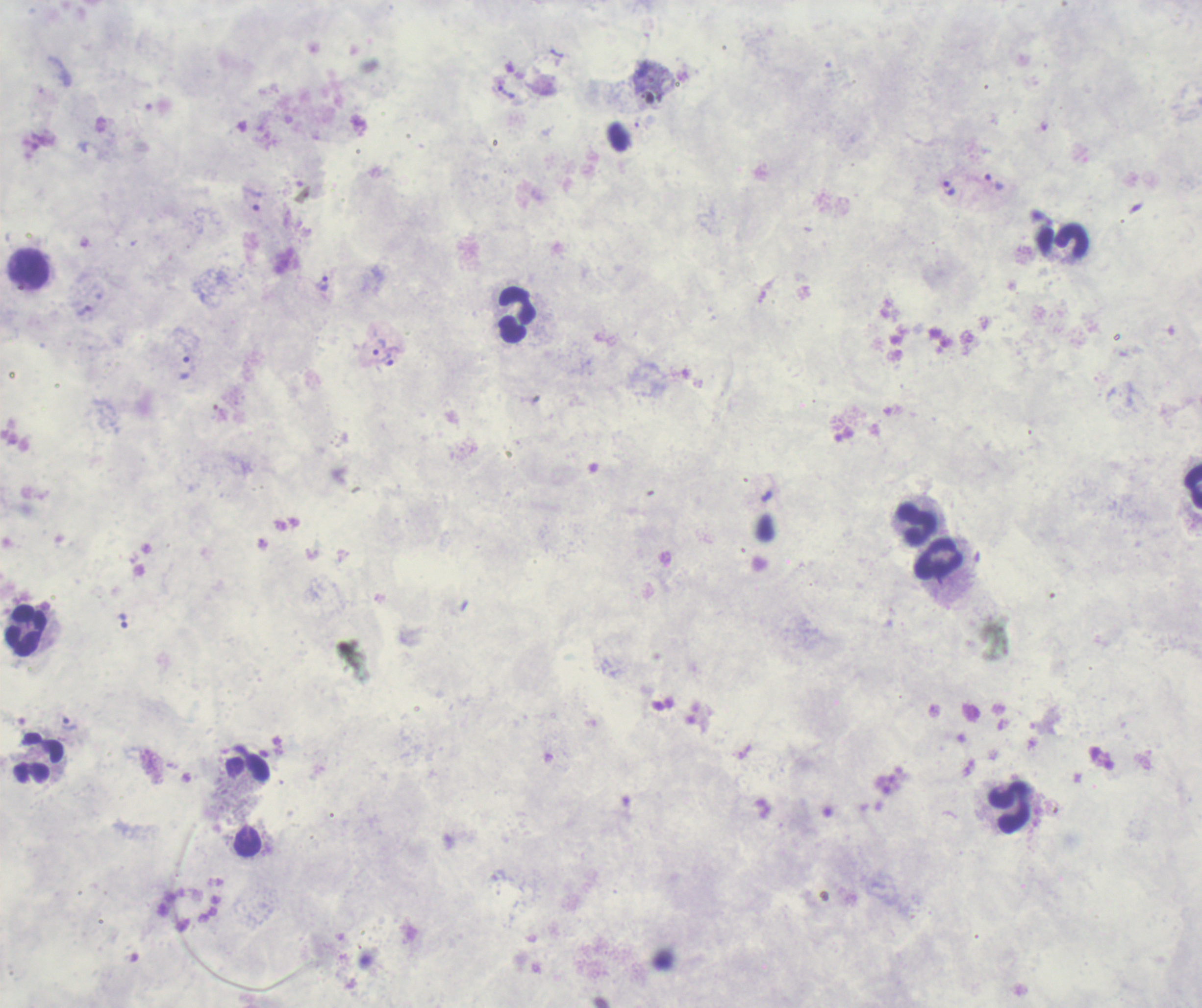
coordinate format = approximate object centers, in pixels from the top-left corner
leukocyte locations = (x=1072, y=241), (x=29, y=268), (x=518, y=315), (x=1193, y=486), (x=916, y=525), (x=939, y=559), (x=27, y=631), (x=39, y=758), (x=249, y=769), (x=1009, y=807)
trophozoite locations = (x=507, y=91), (x=994, y=182), (x=948, y=188), (x=252, y=198), (x=323, y=284), (x=379, y=347), (x=385, y=361), (x=186, y=368), (x=766, y=497), (x=123, y=620), (x=70, y=723)
magnification = 100x
result = malaria parasites identified
stain = Romanowsky
preparation = thick smear of blood
background quality = poor
field of view = one from this slide
context = previously used in a real diagnosis
image size = 1202×1008 pixels